Assess the morphology of the erythrocytes.
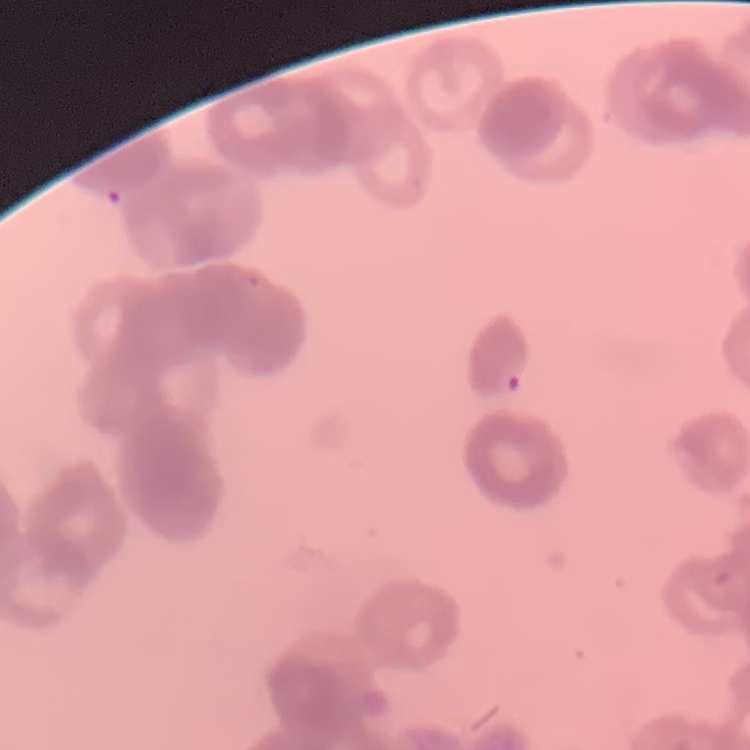
Rouleaux formation.

Summary:
  - Image type: one tile cut from a larger photomicrograph
  - Preparation: thin blood smear
  - Stain: Field's or Giemsa